Give the position of every Plasmodium parasite visible.
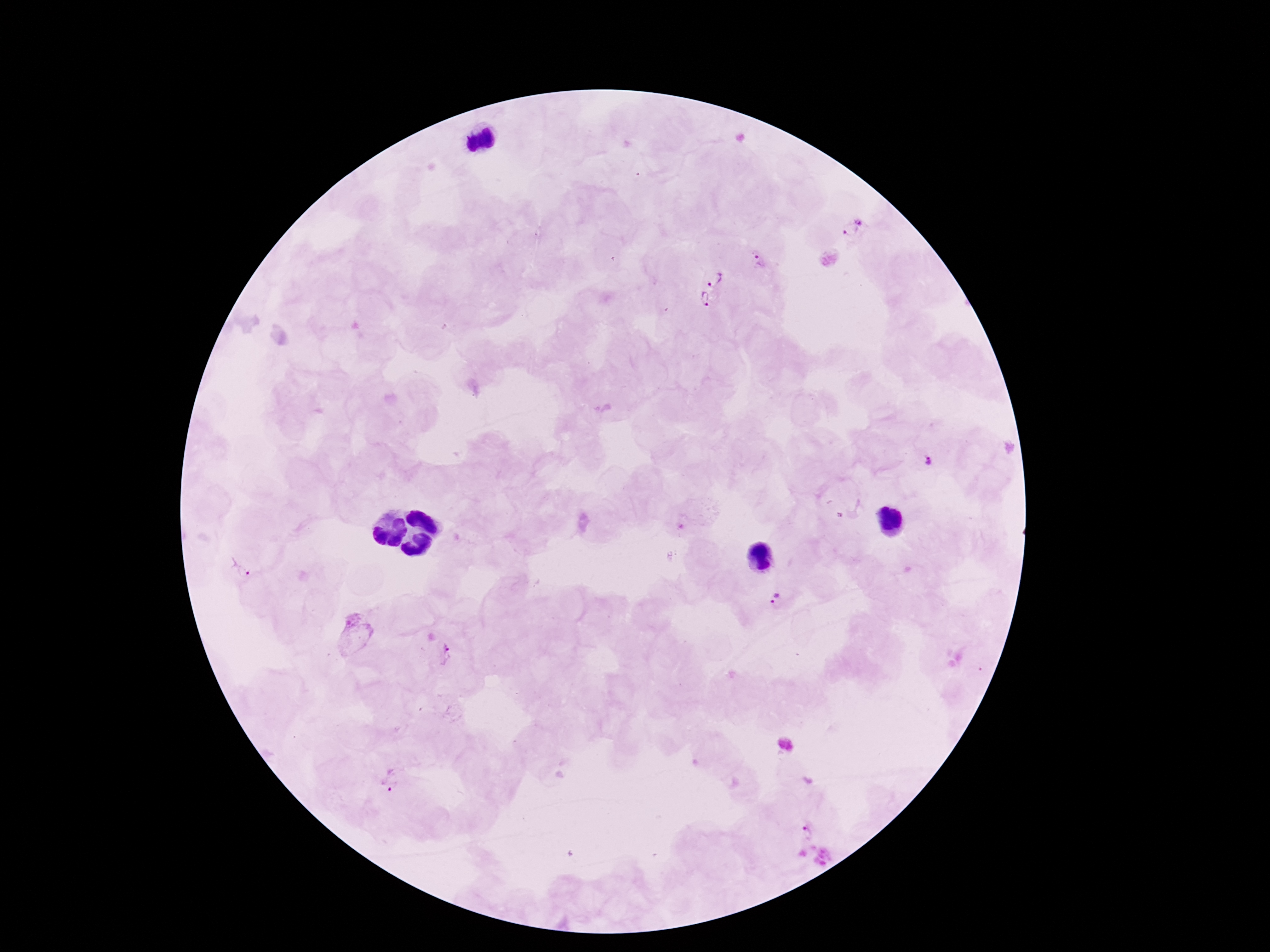
Approximate centers as [x, y] in pixels.
Plasmodium parasites: [861, 218], [851, 230], [759, 262], [713, 278], [705, 299], [927, 462], [243, 570], [779, 602], [450, 655], [390, 780], [807, 833].

capture = smartphone camera through the microscope eyepiece
field of view = single
patient malaria status = infected
image size = 1270×952 pixels
magnification = 100x
stain = Giemsa
preparation = thick blood film